Point out each Plasmodium parasite.
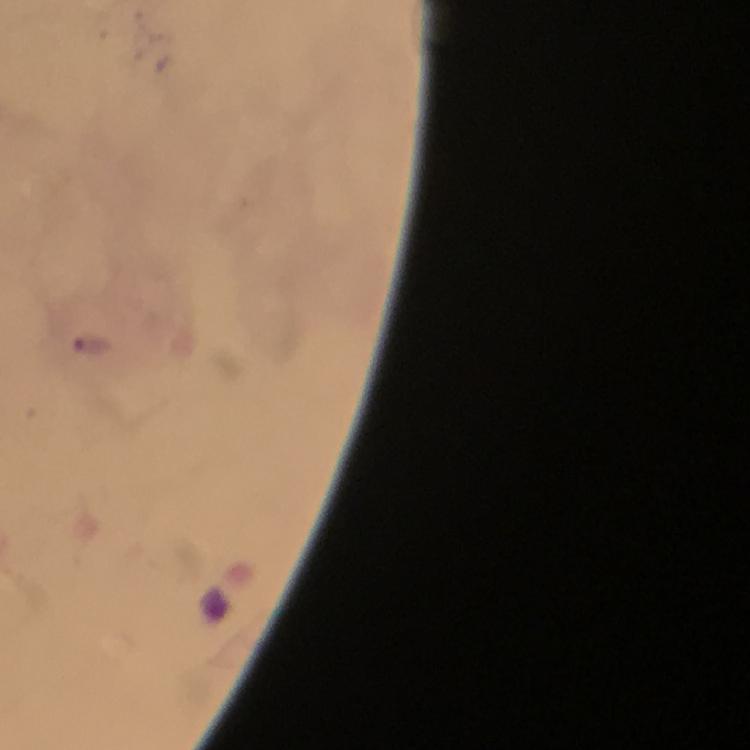

Approximate object centers, in pixels from the top-left corner.
Plasmodium parasites: (x=96, y=343).

Summary:
  - Cropped from: one field of view
  - Stain: Giemsa
  - Preparation: thick blood smear
  - Immersion oil: used
  - Magnification: 100x
  - Context: from a malaria diagnostic workup
  - Image size: 750×750 pixels
  - Capture: smartphone camera through the microscope